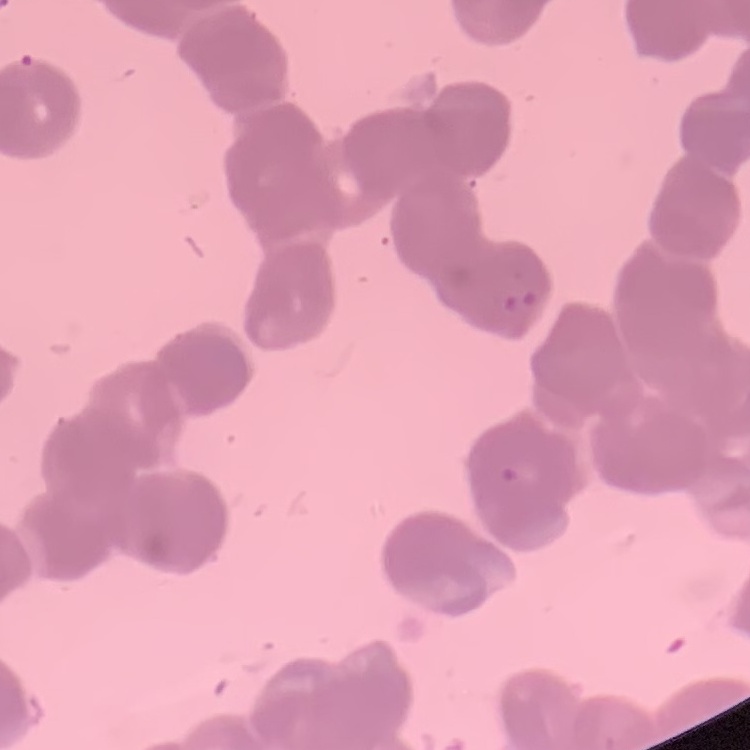

erythrocyte morphology = rouleaux formation
preparation = thin blood film
image type = one tile cut from a larger photomicrograph
stain = Field's or Giemsa